Name the parasite shown.
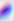
Toxoplasma gondii.

modality = photomicrograph
magnification = 400x